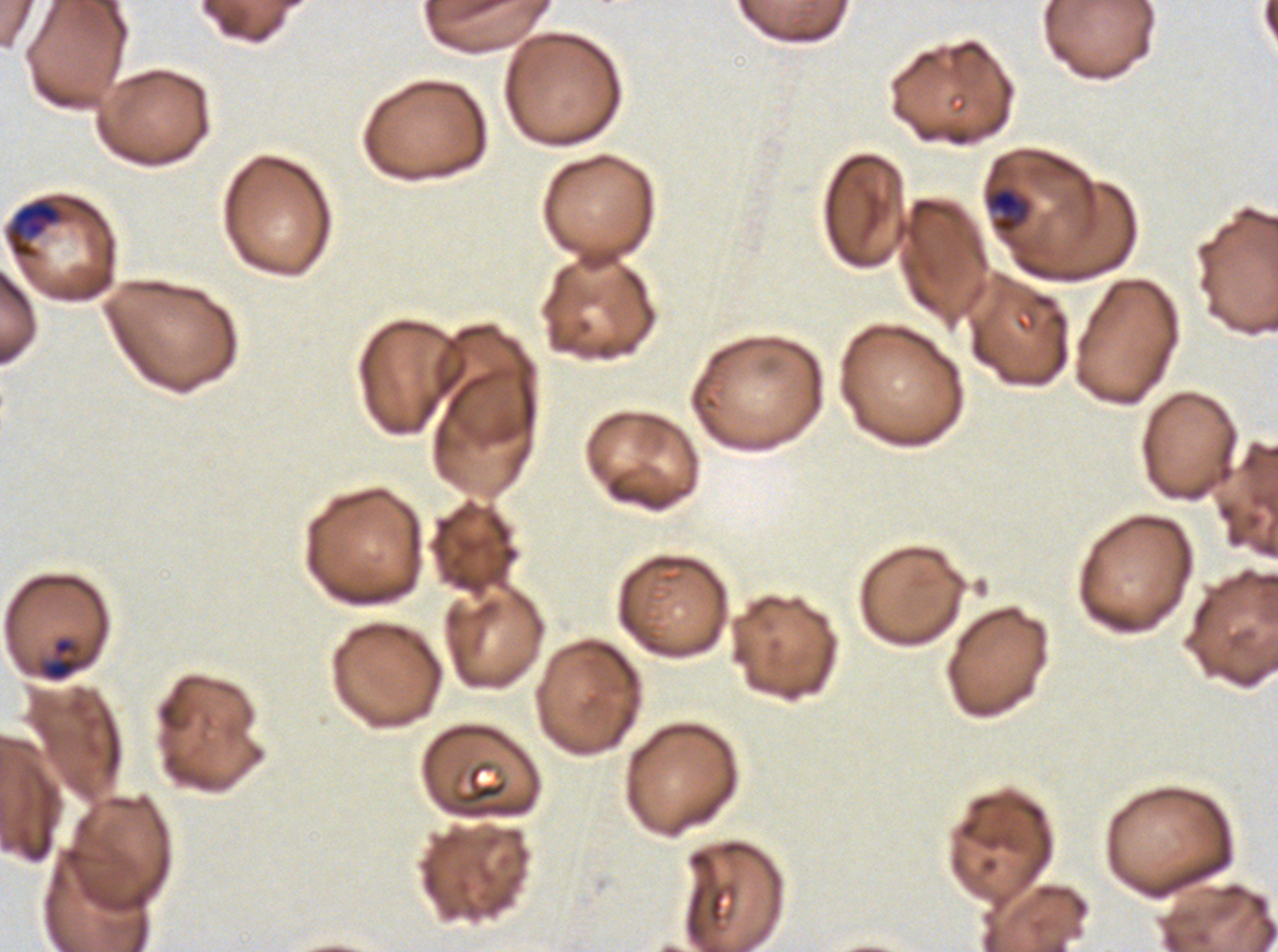
notation = approximate bounding boxes as {x1, y1, x2, y2} in pixels
late-ring/early-trophozoite locations = {988, 187, 1029, 233}, {39, 636, 86, 682}
debris locations = {461, 764, 508, 804}, {708, 890, 725, 922}
late trophozoite locations = {6, 198, 63, 258}
preparation = thin blood smear
image size = 1278×952 pixels
life-cycle stages observed = late-ring/early-trophozoite, late trophozoite
specimen = P. falciparum cultured ex vivo for 24 to 48 hours, from a patient in The Gambia
stain = Giemsa
field of view = sub-image separated from a larger composite